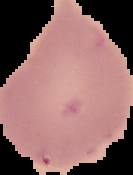
Summary:
  - Image type: cell region segmented out of the field of view; surrounding area masked to black
  - Image size: 133×175 pixels
  - Preparation: thin blood smear
  - Malaria status: uninfected